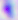
magnification = 400x
modality = photomicrograph
identification = Toxoplasma gondii